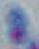
{
  "modality": "photomicrograph",
  "identification": "Toxoplasma gondii",
  "magnification": "1000x"
}